Assess for Plasmodium parasites.
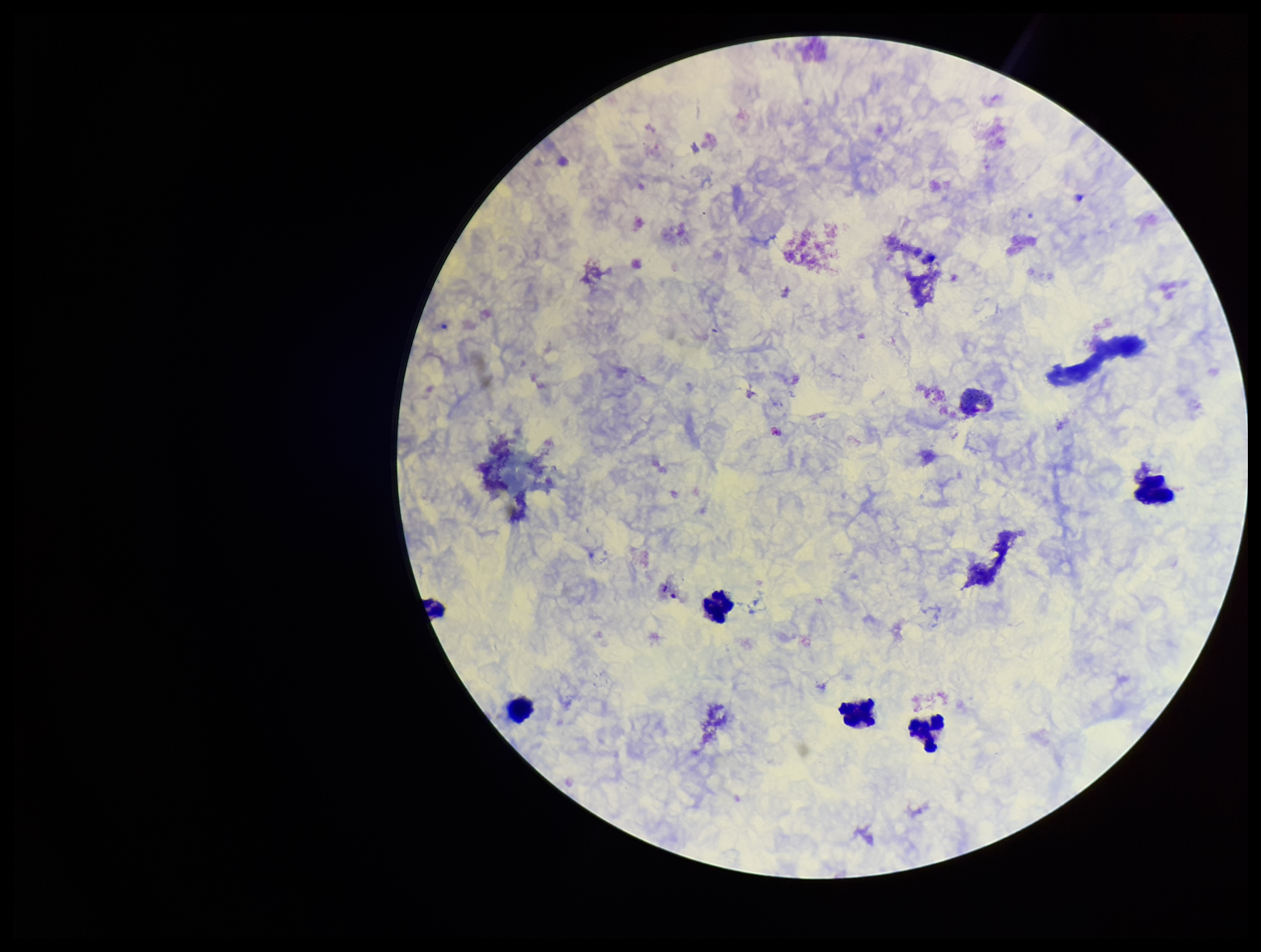

Seen.

stain: Giemsa
field_of_view: one from this slide
leukocyte_count: 7
preparation: thick
parasite_count: 2
capture: smartphone photograph through the microscope eyepiece
image_size: 1261×952 pixels
patient_malaria_status: infected
species_reported_for_this_patient: Plasmodium vivax